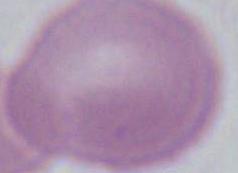
magnification = 1000x
modality = micrograph
identification = red blood cell